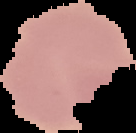
The area outside the segmented cell region is set to black. Malaria status: uninfected. From a thin blood smear. Image is 136×133 pixels.